Classify this cell by malaria status.
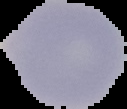

It is uninfected.

Segmented cell region on a black background. Image is 127×109 pixels. From a thin blood smear.